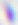

Micrograph. Toxoplasma gondii is shown. 400x magnification.